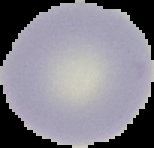
image size = 154×148 pixels
image type = segmented cell region with the area outside set to black
preparation = thin blood smear
result = no malaria parasites seen